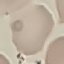 Result: negative for malaria parasites. Photographed with a smartphone camera at the microscope eyepiece. Thin blood smear. Automatically extracted cell patch, resized to 64 × 64 pixels. Giemsa stain.